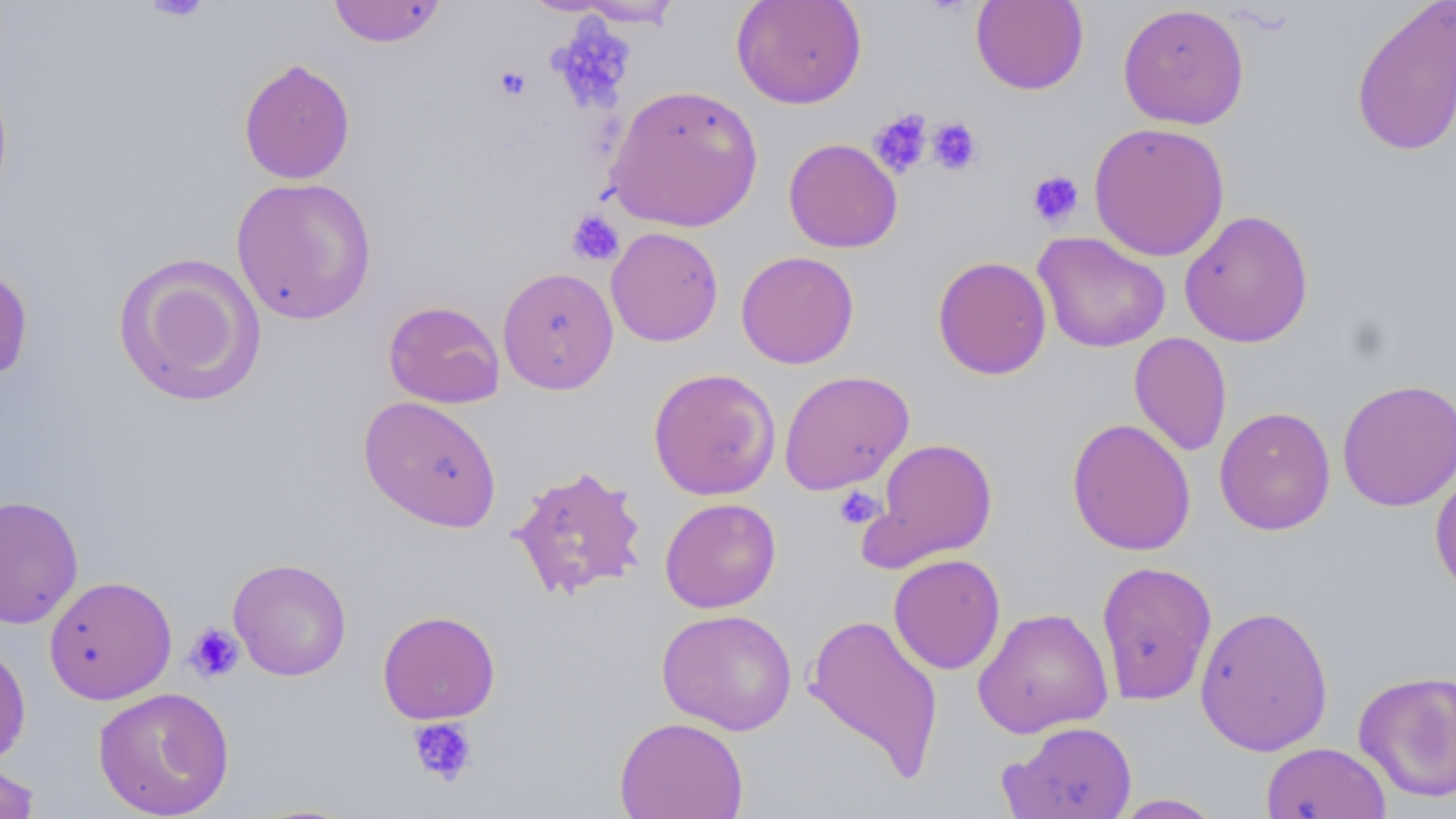
Approximate bounding boxes as named x1/y1/x2/y2 corners in pixels. Uninfected red blood cell locations: (x1=328, y1=0, x2=447, y2=47), (x1=731, y1=0, x2=867, y2=109), (x1=1351, y1=0, x2=1456, y2=157), (x1=571, y1=1, x2=685, y2=28), (x1=970, y1=1, x2=1089, y2=95), (x1=1117, y1=3, x2=1249, y2=129), (x1=238, y1=58, x2=356, y2=184), (x1=0, y1=72, x2=14, y2=210), (x1=605, y1=83, x2=764, y2=233), (x1=1088, y1=121, x2=1230, y2=262), (x1=783, y1=138, x2=903, y2=253), (x1=230, y1=176, x2=377, y2=325), (x1=1179, y1=209, x2=1314, y2=348), (x1=606, y1=226, x2=724, y2=347), (x1=1032, y1=231, x2=1171, y2=353), (x1=735, y1=250, x2=859, y2=369), (x1=113, y1=253, x2=266, y2=407), (x1=932, y1=255, x2=1052, y2=380), (x1=0, y1=262, x2=33, y2=383), (x1=497, y1=266, x2=619, y2=395), (x1=383, y1=300, x2=505, y2=408), (x1=1129, y1=331, x2=1232, y2=457), (x1=647, y1=367, x2=781, y2=500), (x1=778, y1=369, x2=914, y2=495), (x1=1336, y1=378, x2=1456, y2=512), (x1=358, y1=396, x2=503, y2=533), (x1=1214, y1=406, x2=1336, y2=535), (x1=1067, y1=417, x2=1197, y2=556), (x1=867, y1=437, x2=999, y2=568), (x1=1430, y1=462, x2=1456, y2=600), (x1=509, y1=463, x2=649, y2=601), (x1=0, y1=494, x2=84, y2=629), (x1=659, y1=497, x2=782, y2=613), (x1=888, y1=553, x2=1006, y2=675), (x1=227, y1=557, x2=352, y2=681), (x1=1095, y1=559, x2=1218, y2=706), (x1=43, y1=575, x2=177, y2=705), (x1=1195, y1=604, x2=1334, y2=757), (x1=973, y1=606, x2=1113, y2=738), (x1=656, y1=608, x2=797, y2=735), (x1=377, y1=610, x2=500, y2=724), (x1=803, y1=613, x2=945, y2=779), (x1=0, y1=638, x2=32, y2=769), (x1=1353, y1=669, x2=1456, y2=803), (x1=92, y1=686, x2=235, y2=818), (x1=614, y1=715, x2=749, y2=818), (x1=1002, y1=721, x2=1139, y2=819), (x1=1260, y1=742, x2=1392, y2=819), (x1=0, y1=761, x2=42, y2=818), (x1=1109, y1=793, x2=1226, y2=818). Platelet locations: (x1=142, y1=0, x2=212, y2=22), (x1=493, y1=64, x2=532, y2=102), (x1=868, y1=109, x2=933, y2=178), (x1=926, y1=117, x2=983, y2=176), (x1=1026, y1=170, x2=1085, y2=228), (x1=567, y1=209, x2=624, y2=267), (x1=833, y1=486, x2=885, y2=530), (x1=184, y1=622, x2=245, y2=683), (x1=407, y1=718, x2=477, y2=787). Slide-level diagnosis: negative for blood parasites. Thin blood film. Light microscopy. Image is 1456×819 pixels. 1000x magnification. Single field of view. May-Grünwald-Giemsa stain.